Report the malaria status of this cell.
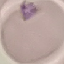
It is uninfected.

preparation: thin smear
capture: smartphone through the microscope eyepiece
image_type: automatically extracted cell patch, resized to 64 × 64 pixels
stain: Giemsa